Report the malaria status of this cell.
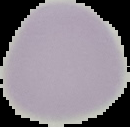
It is uninfected.

Image is 130×127 pixels. Cell region segmented out of the field of view; the surrounding area is masked to black. From a thin blood film.